Assess this cell for malaria.
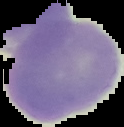

Uninfected.

Image is 124×127 pixels. The area outside the segmented cell region is set to black. From a thin blood smear.